Locate every Plasmodium parasite.
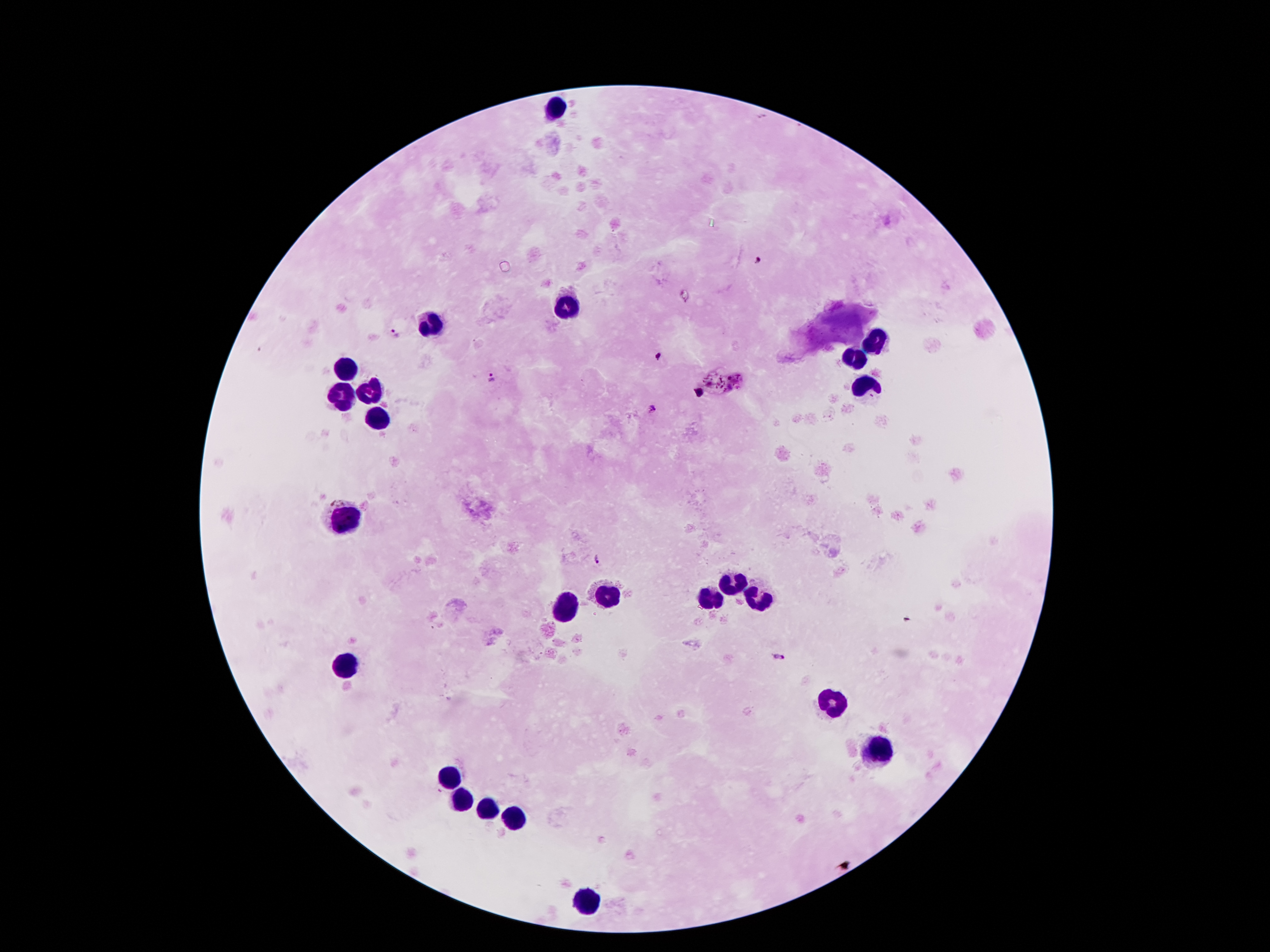
Approximate centers as {x, y} in pixels.
Plasmodium parasites: {756, 260}, {394, 333}, {658, 356}, {490, 379}, {652, 407}, {596, 559}, {779, 657}.

Summary:
  - Leukocyte locations: {556, 103}, {568, 305}, {432, 321}, {873, 344}, {856, 361}, {344, 367}, {375, 386}, {866, 386}, {346, 397}, {379, 420}, {346, 517}, {734, 583}, {610, 596}, {759, 597}, {709, 599}, {566, 609}, {346, 666}, {833, 704}, {879, 748}, {453, 780}, {465, 801}, {486, 809}, {518, 816}, {589, 902}
  - Magnification: 100x
  - Image size: 1270×952 pixels
  - Field of view: single
  - Stain: Giemsa
  - Preparation: thick peripheral-blood smear
  - Patient malaria status: positive for Plasmodium falciparum
  - Capture: smartphone through the microscope eyepiece